Classify this cell by malaria status.
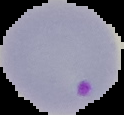
It is parasitized.

From a thin blood smear. Image is 124×115 pixels. Cell region segmented out of the field of view; the surrounding area is masked to black.